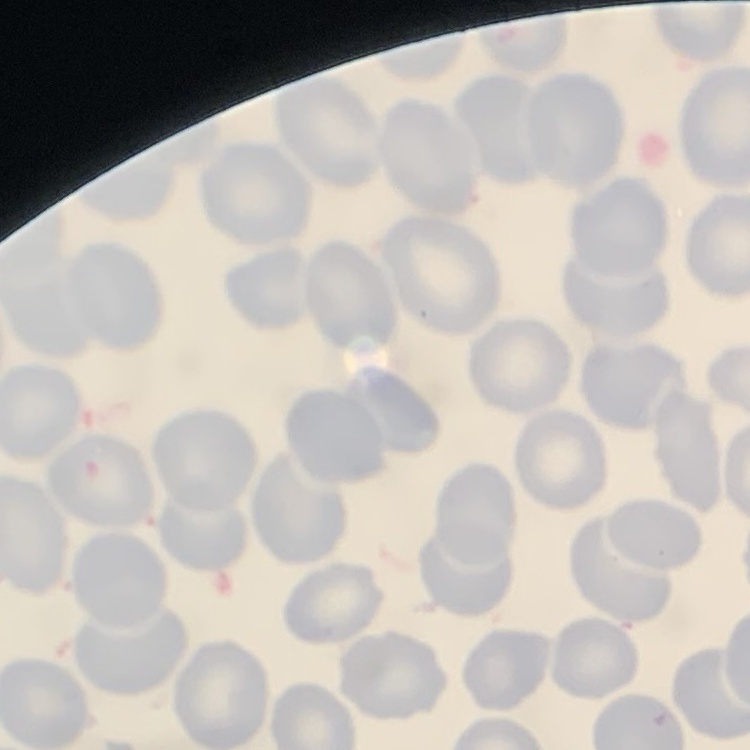 The erythrocytes exhibit no rouleaux formation. One tile cut from a larger photomicrograph. Field's or Giemsa stain. Thin peripheral smear.